Point out each Plasmodium parasite.
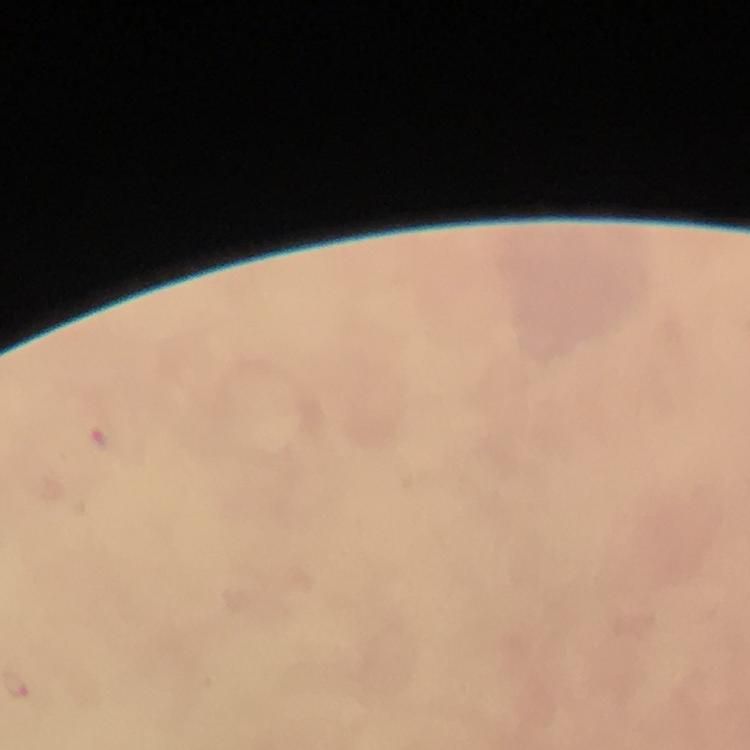
Approximate centers as (x, y) in pixels.
Plasmodium parasites: (105, 440).

Image is 750×750 pixels. Smartphone photograph taken through a microscope. Giemsa stain. At 100x magnification. Thick smear. From a diagnostic examination for malaria. Cropped region of a single field of view. Immersion oil was used.